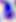
magnification: 400x
modality: photomicrograph
identification: Toxoplasma gondii